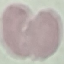

malaria status = uninfected
preparation = thin blood smear
stain = Giemsa
image type = automatically extracted cell patch, resized to 64 × 64 pixels
capture = smartphone camera at the microscope eyepiece